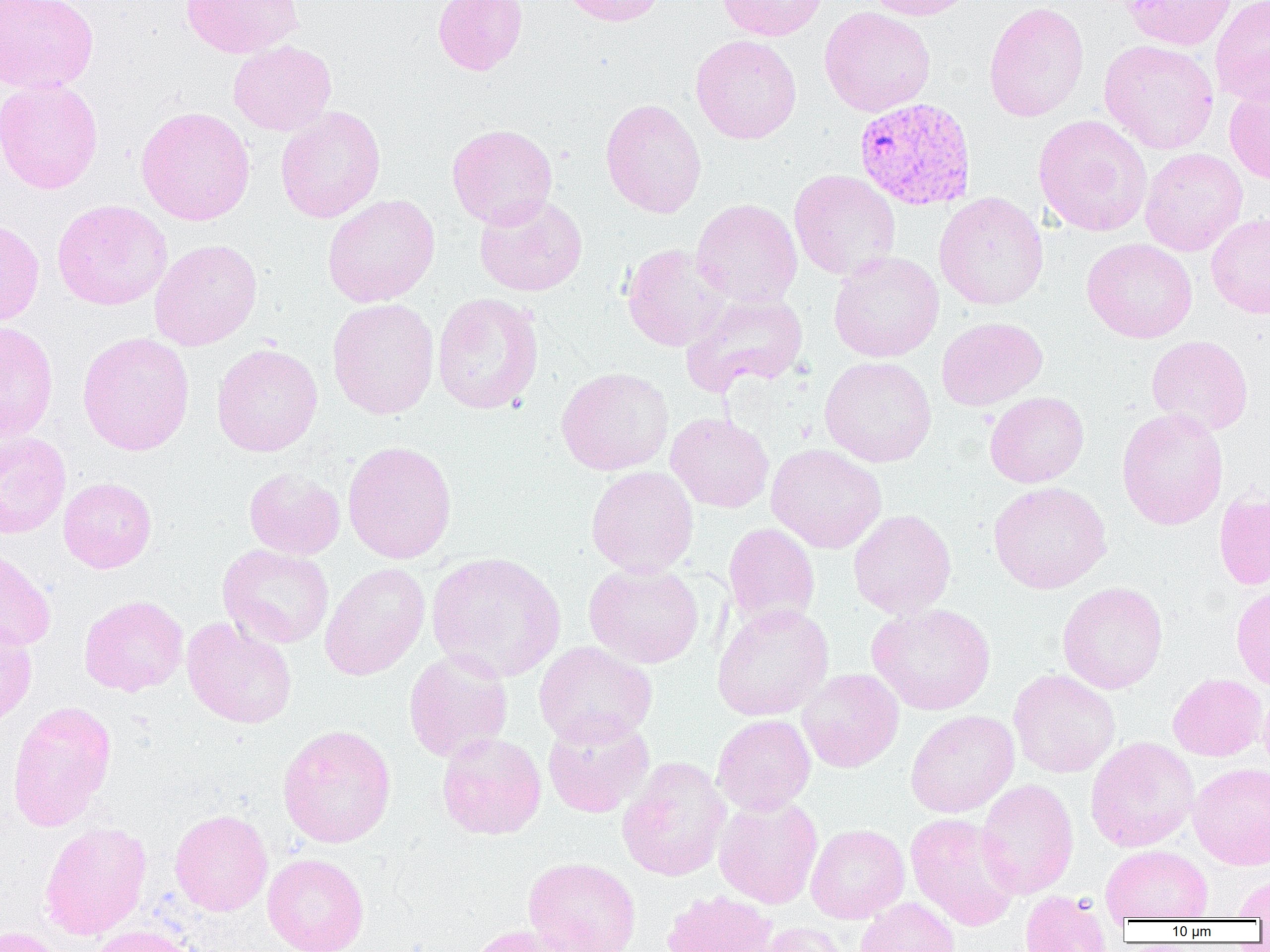

Summary:
  - Coordinate format: approximate bounding boxes as (x1, y1, x2, y2) in pixels
  - Plasmodium vivax-infected red blood cell locations: (853, 97, 977, 210)
  - Uninfected red blood cell locations: (0, 0, 99, 93), (181, 0, 304, 59), (432, 0, 528, 75), (558, 0, 666, 26), (717, 0, 827, 41), (864, 0, 975, 20), (1122, 0, 1236, 51), (1210, 0, 1270, 107), (983, 2, 1089, 122), (819, 6, 936, 117), (690, 34, 802, 144), (1099, 39, 1219, 154), (228, 40, 337, 136), (0, 78, 103, 194), (1224, 83, 1270, 184), (600, 98, 707, 218), (135, 106, 256, 225), (275, 106, 386, 223), (1033, 114, 1153, 237), (447, 123, 558, 229), (1140, 148, 1247, 256), (789, 169, 901, 280), (934, 192, 1049, 310), (322, 194, 440, 307), (474, 194, 587, 297), (52, 199, 173, 310), (691, 199, 803, 308), (1206, 213, 1270, 318), (0, 220, 44, 327), (1082, 238, 1198, 343), (149, 239, 263, 351), (622, 243, 732, 351), (829, 251, 944, 362), (432, 292, 544, 414), (680, 292, 809, 398), (327, 298, 440, 420), (936, 316, 1047, 411), (0, 321, 59, 442), (77, 331, 195, 456), (1146, 335, 1254, 435), (211, 343, 323, 457), (819, 355, 936, 467), (555, 366, 674, 476), (985, 391, 1089, 488), (1116, 407, 1228, 530), (665, 412, 774, 513), (0, 431, 71, 539), (342, 440, 457, 564), (765, 443, 887, 553), (586, 465, 699, 577), (244, 467, 345, 560), (59, 477, 157, 573), (988, 482, 1112, 594), (1214, 490, 1270, 589), (848, 509, 956, 618), (723, 522, 820, 630), (217, 544, 334, 648), (0, 546, 56, 652), (427, 551, 566, 682), (583, 561, 704, 668), (320, 562, 430, 680), (1057, 582, 1168, 694), (1231, 583, 1270, 690), (79, 594, 189, 697), (712, 602, 834, 721), (867, 602, 996, 715), (181, 617, 297, 729), (0, 622, 37, 727), (534, 641, 657, 747), (403, 650, 514, 762), (797, 668, 904, 773), (1008, 668, 1120, 778), (1168, 673, 1267, 761), (1258, 684, 1270, 778), (7, 700, 117, 832), (905, 709, 1019, 818), (542, 712, 655, 818), (712, 714, 816, 815), (277, 723, 397, 848), (437, 732, 546, 839), (1085, 736, 1200, 852), (617, 756, 731, 882), (1188, 762, 1270, 870), (976, 778, 1078, 899), (713, 795, 823, 909), (169, 809, 272, 916), (905, 812, 1022, 932), (39, 821, 152, 940), (806, 824, 910, 923), (1100, 844, 1213, 922), (262, 853, 369, 952), (523, 857, 642, 952), (1232, 874, 1270, 920), (661, 889, 779, 952), (1019, 890, 1111, 952), (854, 897, 961, 952), (755, 921, 853, 952), (465, 924, 579, 952), (86, 925, 202, 952), (0, 926, 67, 952)
  - Slide-level diagnosis: Plasmodium vivax
  - Preparation: thin blood smear
  - Modality: optical microscopy
  - Image size: 1270×952 pixels
  - Field of view: one of a larger specimen
  - Magnification: 1000x